Report the malaria status.
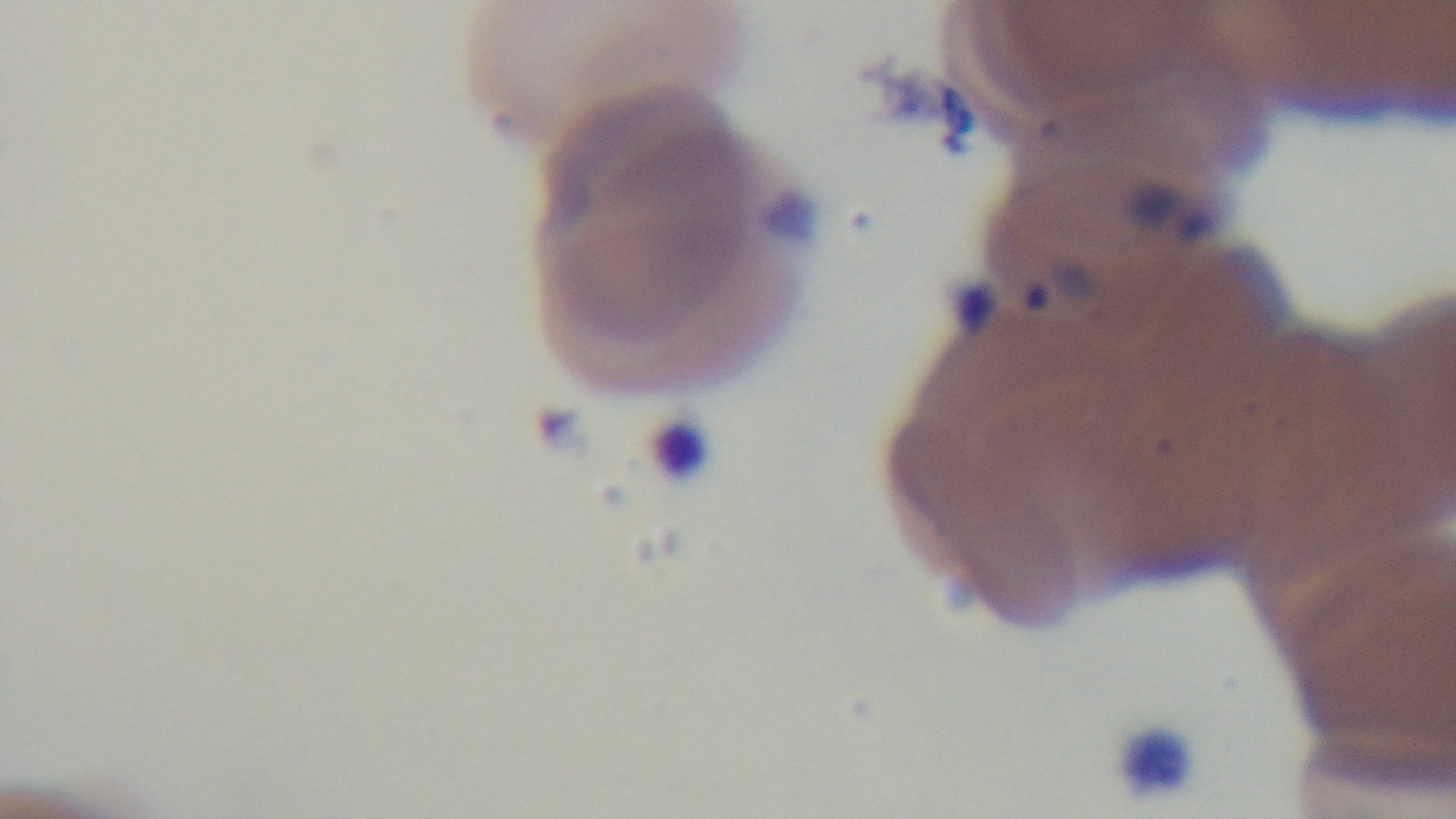

It is infected.

objective: 100x oil immersion
capture: mounted 4K digital camera
stain: Giemsa
preparation: thin blood film
modality: light microscopy
field_of_view: one from the slide